Assess this cell for malaria.
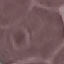
Uninfected.

Summary:
  - Image type: cell patch, automatically extracted from a larger field of view and resized to 64 × 64 pixels
  - Preparation: thin blood film
  - Capture: smartphone camera at the microscope eyepiece
  - Stain: Giemsa